Give the position of every Plasmodium parasite.
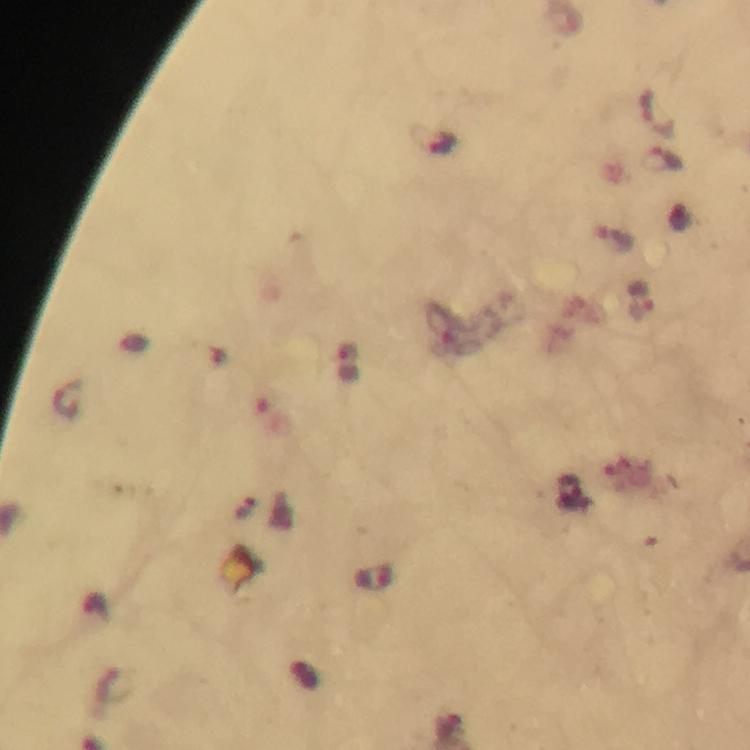

Approximate centers as [x, y] in pixels.
Plasmodium parasites: [657, 112], [434, 140], [661, 158], [642, 301], [572, 494], [373, 579].

preparation = thick blood film
stain = Giemsa
context = from a malaria diagnostic workup
magnification = 100x
immersion oil = applied
capture = smartphone camera through the microscope
image size = 750×750 pixels
cropped from = a single field of view